Comment on the morphology of the red blood cells.
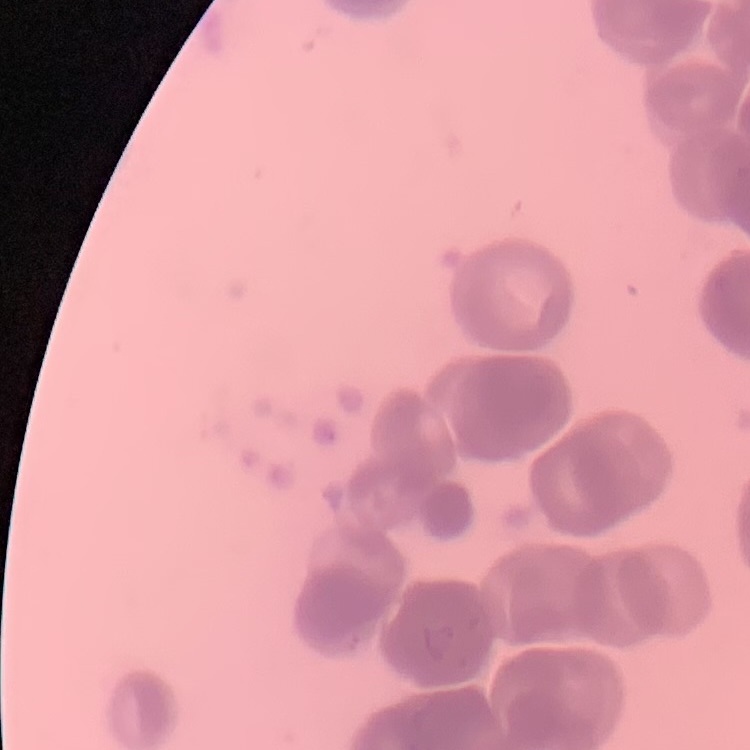

Rouleaux formation.

Field's or Giemsa stain. One tile cut from a larger photomicrograph. Thin blood smear.